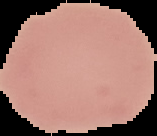

preparation = thin blood film
image size = 157×136 pixels
result = negative for Plasmodium parasites
image type = segmented cell region on a black background